Outline every parasitised red blood cell, every trophozoite, every gametocyte, every leukocyte, and every artifact (platelet-like body, stain precipitate, or debris).
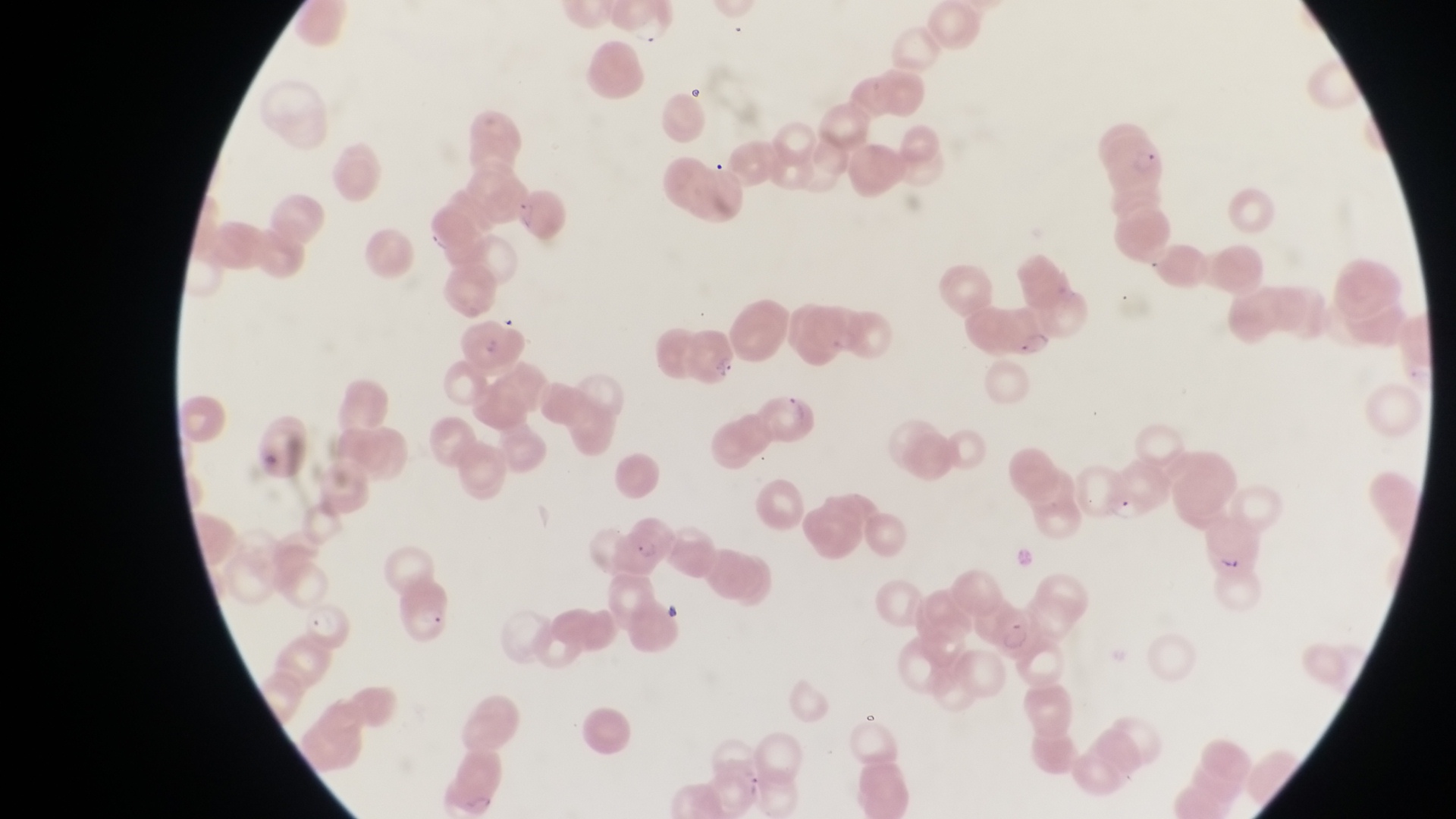

Approximate bounding boxes as {left, top, right, bottom} in pixels.
Parasitised red blood cells: {1102, 130, 1169, 193}, {990, 298, 1063, 367}, {680, 325, 743, 389}, {978, 597, 1037, 655}.
Trophozoites: {303, 602, 352, 647}.
No leukocytes observed.

magnification: 1000x
image_size: 1456×819 pixels
country: Uganda
capture: smartphone photograph through the eyepiece of an Olympus CX-23 microscope
preparation: thin blood smear
field_of_view: single